Assess the morphology of the erythrocytes.
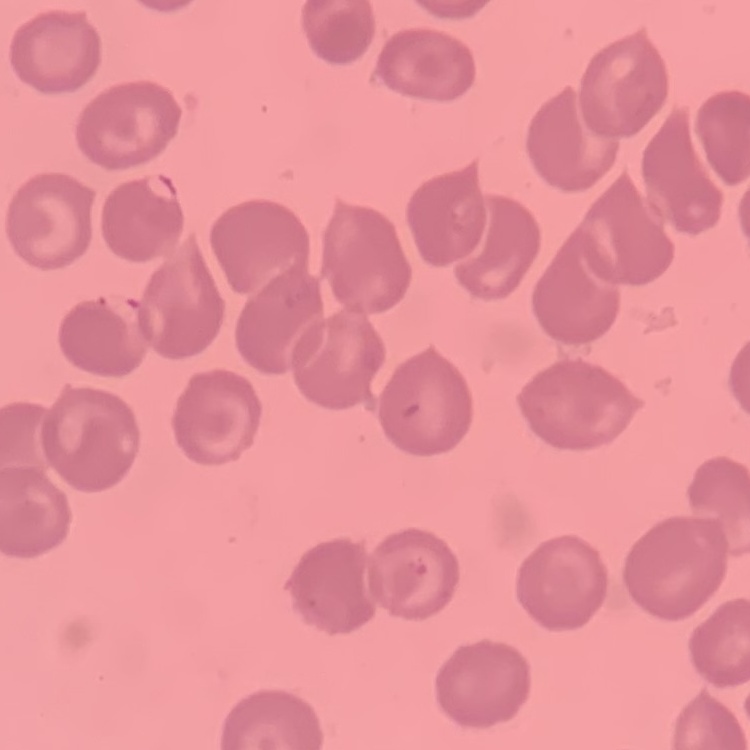
No rouleaux formation.

Thin blood film. One tile cut from a larger photomicrograph. Field's or Giemsa stain.